Locate every Plasmodium parasite.
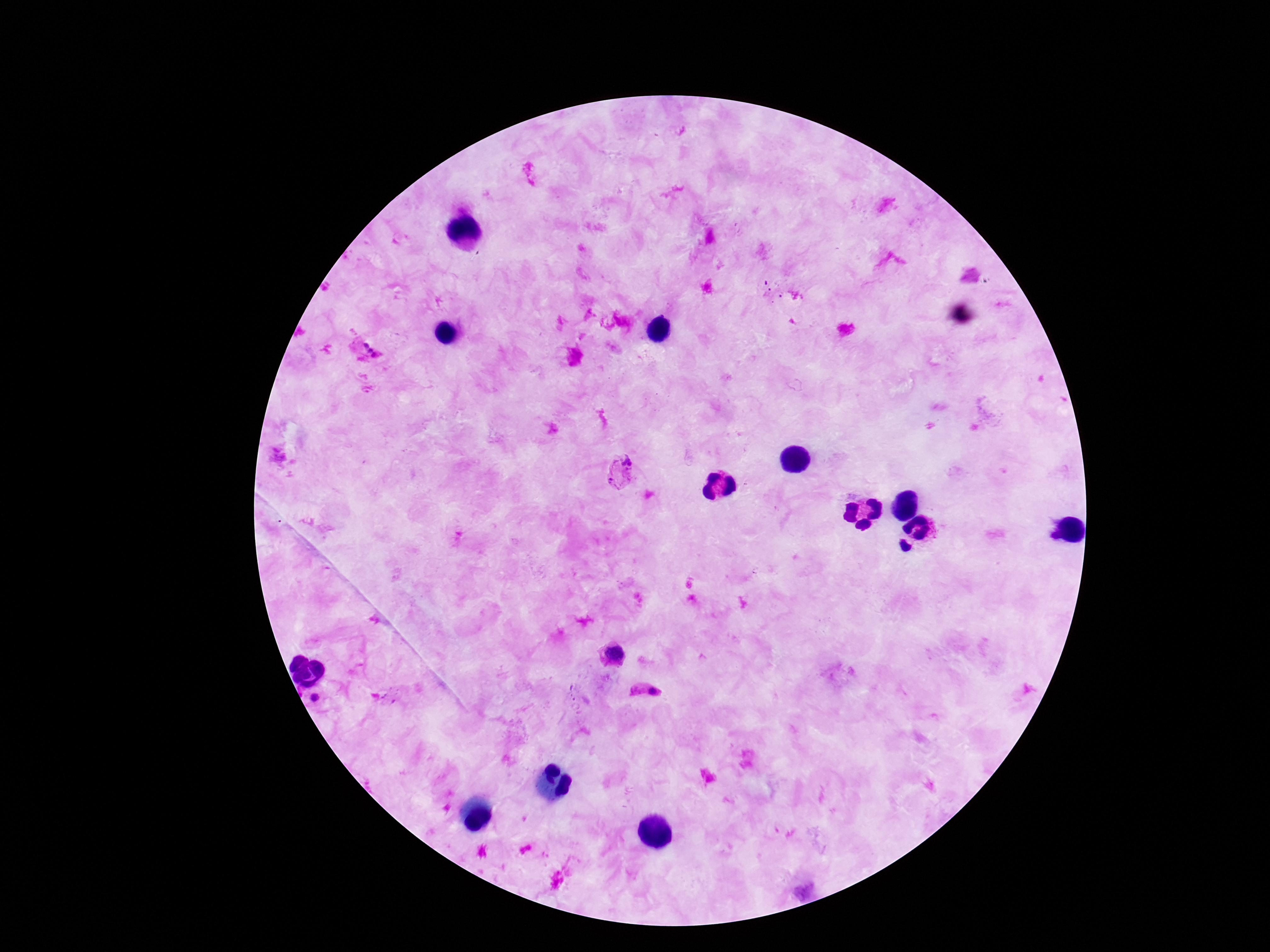
Approximate centers as {x, y} in pixels.
Plasmodium parasites: {370, 352}, {627, 462}, {613, 482}, {613, 657}, {647, 691}, {315, 699}.

Image is 1270×952 pixels. Smartphone photograph taken through the microscope eyepiece. One field from this slide. Thick peripheral-blood smear. Patient malaria status: positive. Giemsa-stained preparation. 100x magnification.